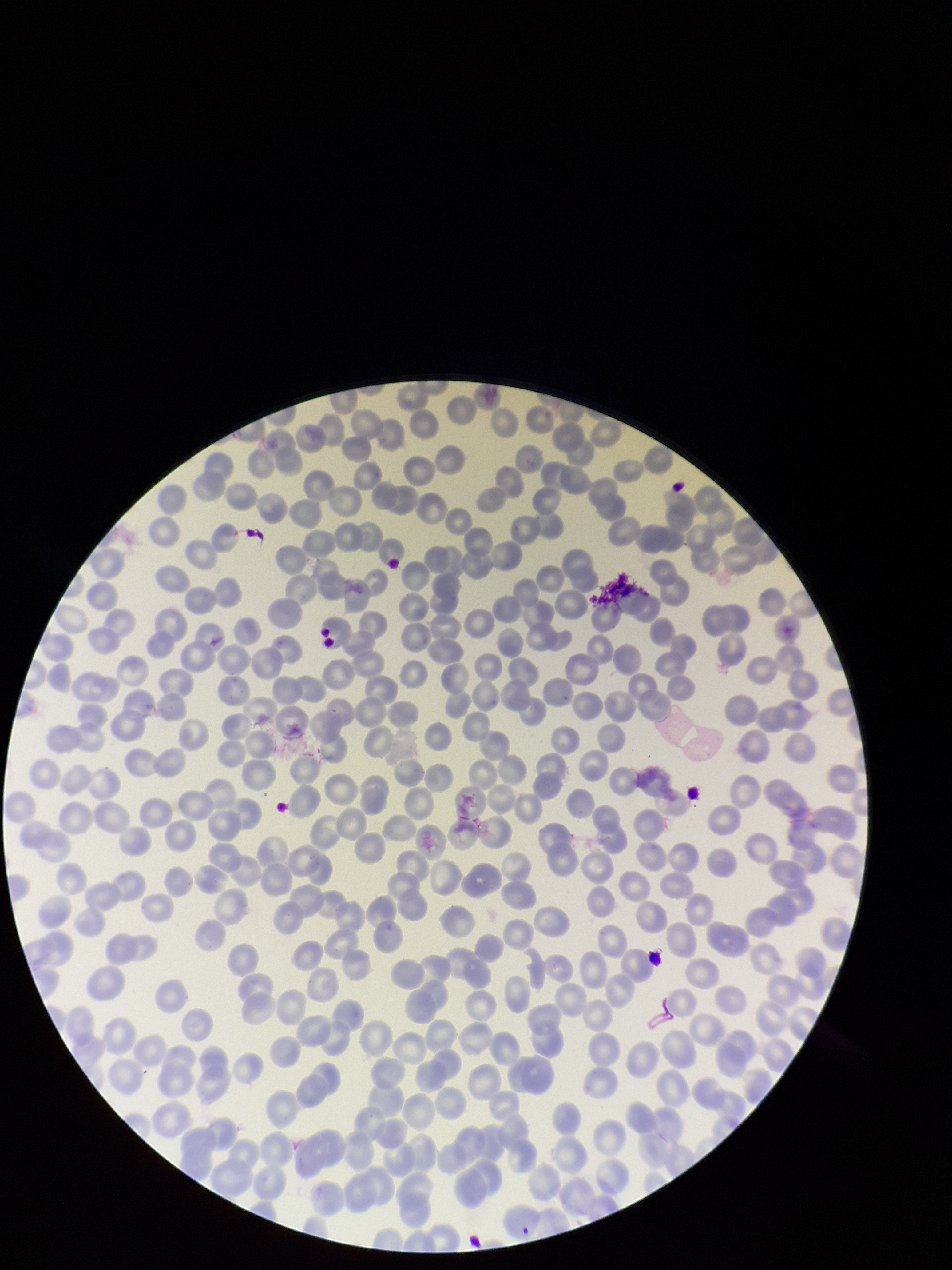

{
  "parasitized_red_blood_cell_count": 0,
  "stain": "Giemsa",
  "capture": "smartphone photograph through the microscope eyepiece",
  "image_size": "952×1270 pixels",
  "field_of_view": "single",
  "patient_malaria_status": "infected",
  "preparation": "thin blood smear",
  "species_reported_for_this_patient": "Plasmodium falciparum",
  "parasitized_red_blood_cells": "none seen",
  "red_blood_cell_count": 272
}